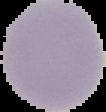
result = no malaria parasites seen
preparation = thin blood film
image size = 106×112 pixels
image type = segmented cell region on a black background